Assess this cell for malaria.
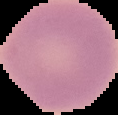

It is uninfected.

From a thin blood smear. The area outside the segmented cell region is set to black. Image is 118×115 pixels.